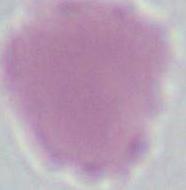
Photomicrograph. A red blood cell is seen. 1000x magnification.